Give the position of every Plasmodium parasite.
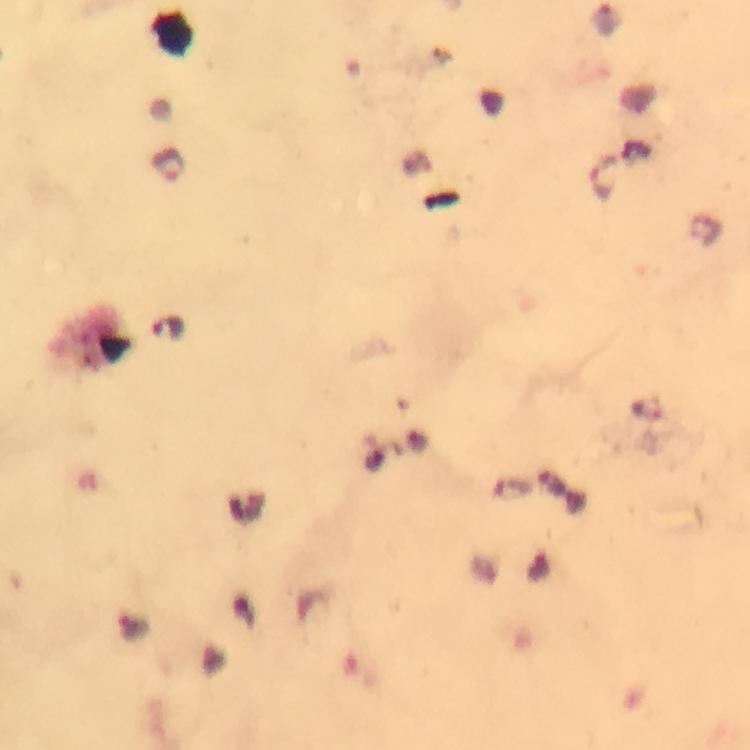

Approximate centers as (x, y) in pixels.
Plasmodium parasites: (168, 164), (603, 179), (511, 489).

Thick blood film. Immersion oil was used. Image is 750×750 pixels. Cropped region of a single field of view. Giemsa-stained preparation. Smartphone photograph taken through a microscope. From a malaria diagnostic workup. At 100x magnification.